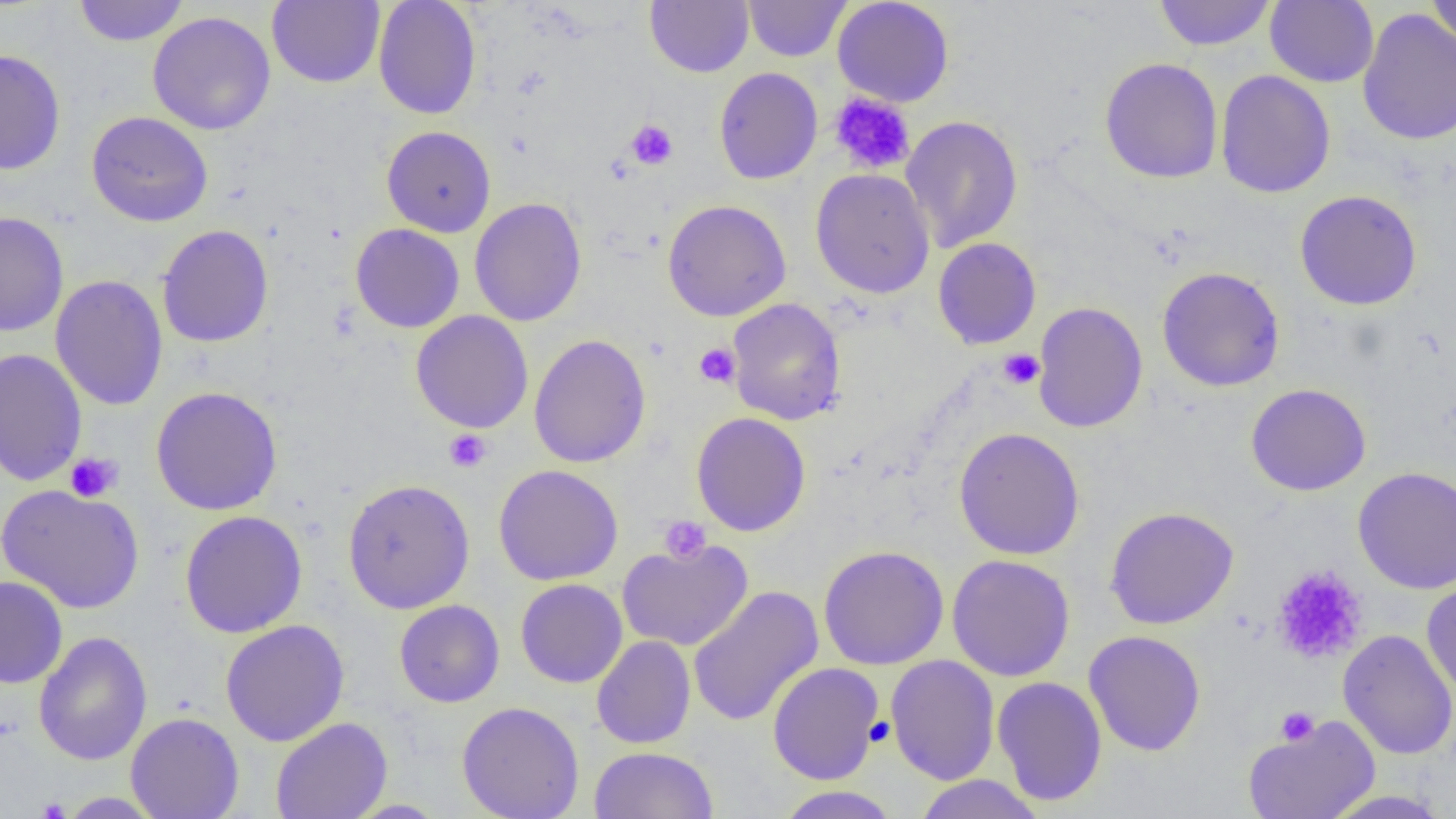

slide-level diagnosis = negative for blood parasites
modality = light microscopy
magnification = 1000x
image size = 1456×819 pixels
preparation = thin blood film
field of view = one of a larger specimen
uninfected red blood cell locations = approximate bounding boxes as (x1, y1, x2, y2) in pixels: (74, 0, 189, 47), (267, 0, 385, 88), (373, 0, 482, 120), (645, 0, 753, 77), (743, 0, 851, 61), (833, 0, 954, 107), (1153, 0, 1275, 51), (1265, 1, 1379, 88), (1426, 1, 1456, 48), (1357, 8, 1456, 145), (147, 11, 276, 135), (0, 48, 66, 176), (1099, 57, 1223, 183), (714, 67, 823, 184), (1215, 70, 1336, 198), (86, 111, 213, 227), (900, 115, 1023, 253), (381, 125, 496, 237), (811, 168, 935, 299), (1295, 189, 1423, 311), (469, 198, 587, 327), (662, 199, 791, 321), (0, 211, 69, 337), (351, 223, 465, 333), (156, 224, 274, 348), (933, 237, 1042, 349), (1157, 266, 1285, 393), (51, 275, 168, 411), (727, 298, 846, 426), (1032, 301, 1148, 433), (410, 311, 534, 433), (528, 334, 651, 468), (0, 347, 87, 487), (1245, 383, 1371, 496), (151, 386, 282, 515), (691, 412, 811, 537), (953, 427, 1086, 560), (494, 464, 623, 586), (1353, 467, 1456, 594), (342, 478, 476, 614), (0, 483, 145, 614), (1104, 506, 1239, 630), (179, 510, 308, 638), (616, 539, 754, 652), (818, 544, 949, 670), (946, 554, 1075, 681), (1269, 564, 1366, 661), (0, 575, 68, 688), (515, 579, 628, 688), (1421, 579, 1456, 699), (687, 586, 824, 727), (394, 600, 505, 707), (220, 619, 350, 746), (1337, 629, 1456, 760), (1084, 630, 1206, 756), (33, 631, 153, 766), (591, 635, 696, 749), (885, 654, 1000, 785), (768, 662, 884, 785), (991, 676, 1107, 806), (457, 701, 585, 819), (126, 712, 245, 819), (1242, 715, 1381, 819), (271, 717, 393, 819), (588, 746, 719, 818), (912, 774, 1046, 819), (774, 786, 901, 818), (1319, 789, 1453, 818), (55, 792, 164, 818), (342, 798, 450, 818)
platelet locations = approximate bounding boxes as (x1, y1, x2, y2) in pixels: (829, 92, 915, 175), (625, 120, 678, 170), (694, 342, 741, 388), (998, 348, 1044, 390), (444, 429, 492, 472), (64, 451, 123, 502), (658, 515, 713, 564), (1270, 566, 1368, 664), (1276, 707, 1319, 746), (866, 717, 895, 746)